Classify this cell by malaria status.
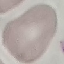

It is uninfected.

Giemsa stain. Cell patch, automatically extracted from a larger field of view and resized to 64 × 64 pixels. Acquired by smartphone through the microscope eyepiece. Thin smear of blood.